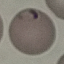
Result: malaria parasites identified. Giemsa-stained preparation. Thin blood film. Acquired by smartphone through the microscope eyepiece. Cell patch, automatically extracted from a larger field of view and resized to 64 × 64 pixels.